Point out each malaria parasite.
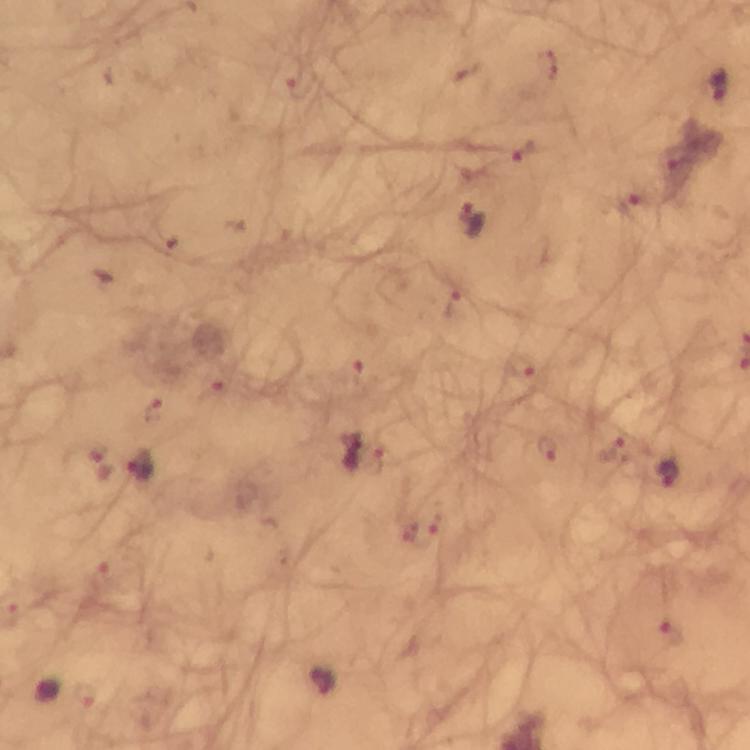

Approximate centers as (x, y) in pixels.
Malaria parasites: (547, 66), (293, 78), (717, 86), (526, 152), (679, 159), (630, 201), (471, 220), (448, 304), (521, 366), (356, 367), (215, 393), (153, 409), (546, 448), (354, 451), (610, 451), (97, 460), (142, 467), (667, 474), (421, 531), (99, 571), (672, 633), (322, 683).

{
  "context": "from a diagnostic examination for malaria",
  "preparation": "thick blood smear",
  "image_size": "750×750 pixels",
  "capture": "smartphone photograph through a microscope",
  "cropped_from": "a single field of view",
  "immersion_oil": "used",
  "stain": "Giemsa",
  "magnification": "100x"
}